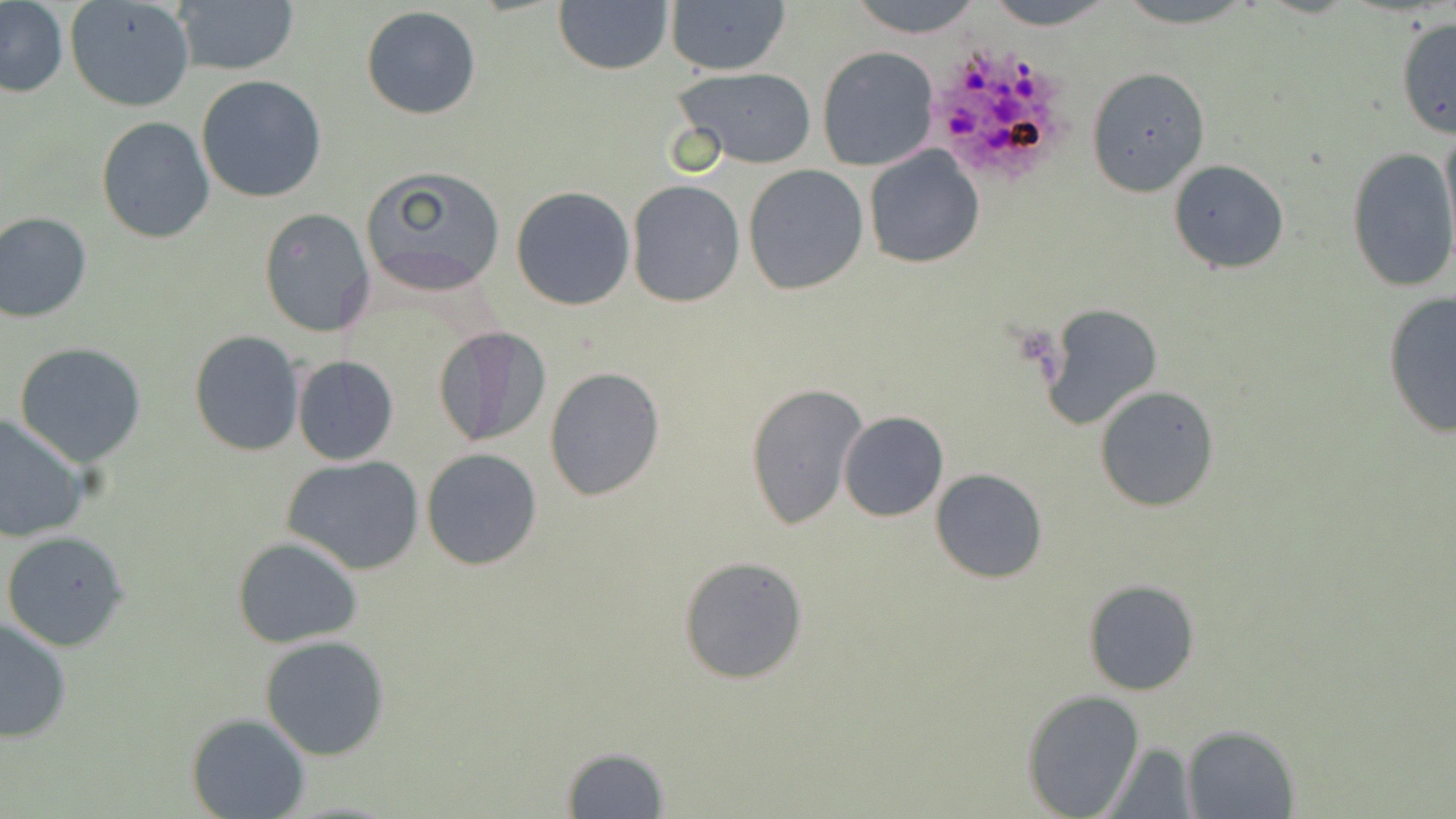
Approximate bounding boxes as (x1, y1, x2, y2) in pixels. Plasmodium ovale-infected red blood cell locations: (929, 41, 1074, 190). Uninfected red blood cell locations: (65, 0, 195, 112), (172, 0, 300, 75), (553, 0, 673, 76), (664, 0, 792, 76), (846, 0, 984, 39), (980, 0, 1122, 27), (1107, 0, 1269, 28), (0, 3, 69, 98), (361, 5, 482, 120), (1394, 15, 1455, 140), (817, 45, 940, 170), (672, 67, 818, 167), (1086, 67, 1211, 197), (196, 76, 327, 204), (96, 117, 215, 243), (862, 146, 985, 267), (1345, 146, 1456, 294), (1168, 160, 1289, 275), (359, 165, 507, 295), (742, 165, 870, 295), (627, 180, 745, 305), (511, 186, 635, 310), (259, 208, 375, 338), (0, 212, 92, 322), (1381, 292, 1456, 439), (1042, 304, 1162, 429), (432, 324, 551, 449), (189, 330, 305, 457), (14, 343, 147, 466), (291, 355, 399, 465), (544, 367, 666, 503), (744, 380, 867, 531), (1094, 384, 1220, 513), (838, 411, 948, 522), (0, 412, 91, 541), (421, 448, 542, 569), (283, 455, 425, 574), (931, 468, 1049, 584), (2, 529, 131, 650), (231, 536, 365, 649), (678, 555, 809, 685), (1083, 578, 1200, 696), (0, 616, 73, 743), (258, 634, 390, 760), (1022, 688, 1145, 816), (185, 711, 310, 819), (1180, 725, 1299, 818), (1101, 742, 1196, 816), (558, 746, 672, 817). Slide-level diagnosis: Plasmodium ovale. Thin blood film. May-Grünwald-Giemsa-stained preparation. One field of a larger specimen. Optical microscopy. Image is 1456×819 pixels. Captured at 1000x magnification.